Assess this cell for malaria.
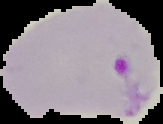
Parasitized.

From a thin blood smear. Image is 163×124 pixels. The area outside the segmented cell region is set to black.